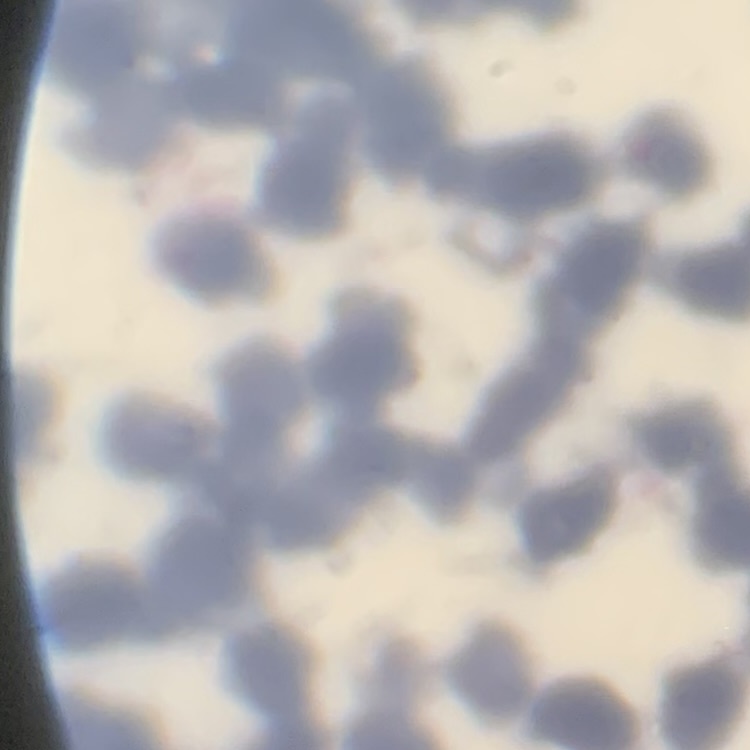

erythrocyte morphology = rouleaux formation
stain = Field's or Giemsa
preparation = thin blood film
image type = square crop of a larger photomicrograph